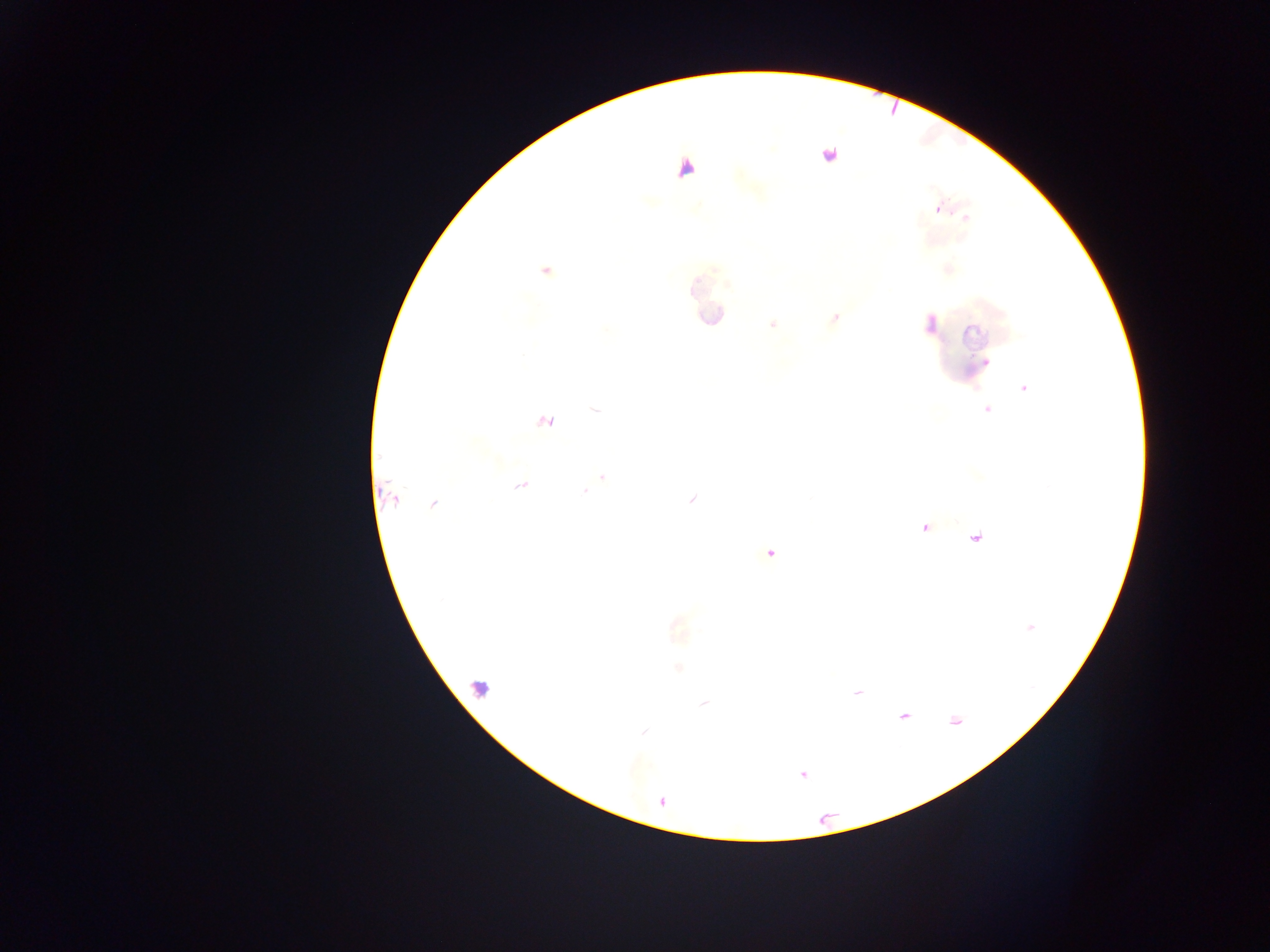
Approximate centers as {x, y} in pixels.
Summary:
  - Malaria parasite locations: {828, 155}, {938, 209}, {965, 217}, {545, 272}, {835, 317}, {772, 324}, {1024, 388}, {987, 410}, {596, 411}, {545, 422}, {603, 477}, {521, 485}, {585, 491}, {394, 499}, {691, 500}, {433, 504}, {770, 553}, {1030, 627}, {677, 628}, {678, 667}, {856, 692}, {704, 704}, {903, 716}, {954, 720}, {643, 731}, {803, 774}
  - Leukocyte locations (subset; some below the resolvable size): {479, 688}
  - Capture: mobile-phone photograph through a microscope
  - Country: Ghana
  - Image size: 1270×952 pixels
  - Preparation: thick blood smear
  - Field of view: single